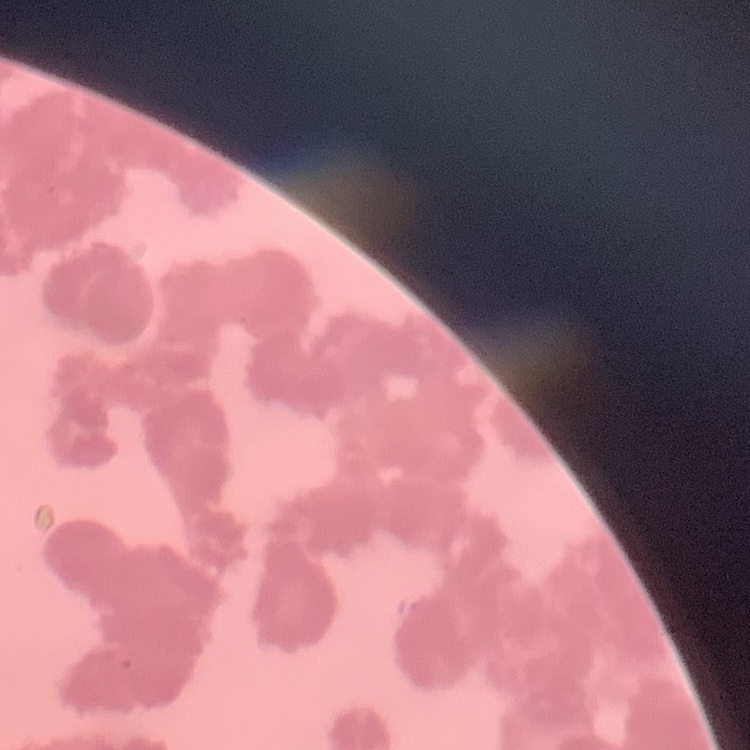

erythrocyte_morphology: rouleaux formation
image_type: square crop of a larger photomicrograph
stain: Field's or Giemsa
preparation: thin blood film